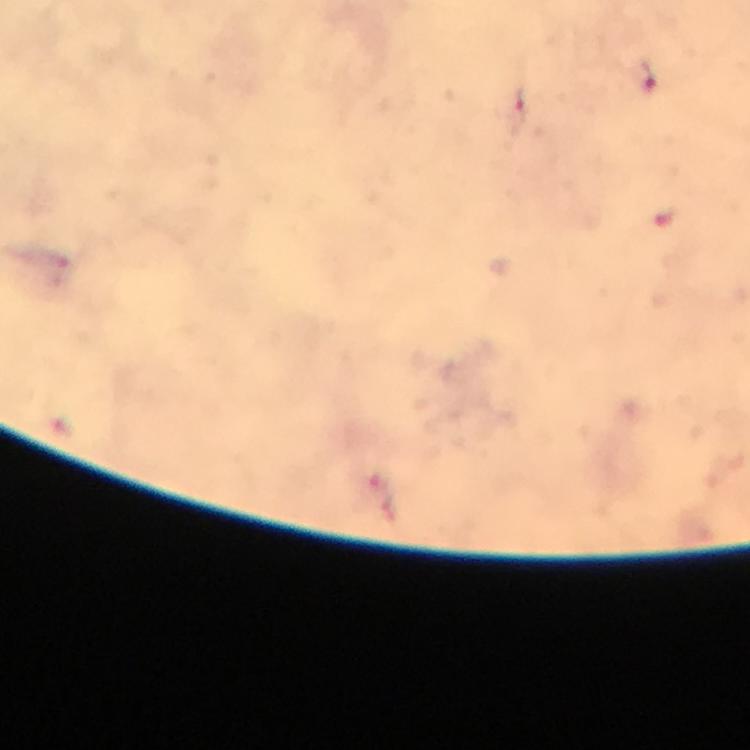
Approximate centers as [x, y] in pixels. Plasmodium parasite locations: [645, 76], [518, 108], [664, 217]. Image is 750×750 pixels. From a malaria diagnostic workup. At 100x magnification. Giemsa stain. Smartphone photograph taken through a microscope. Thick smear. A crop from one field of view. Immersion oil applied.